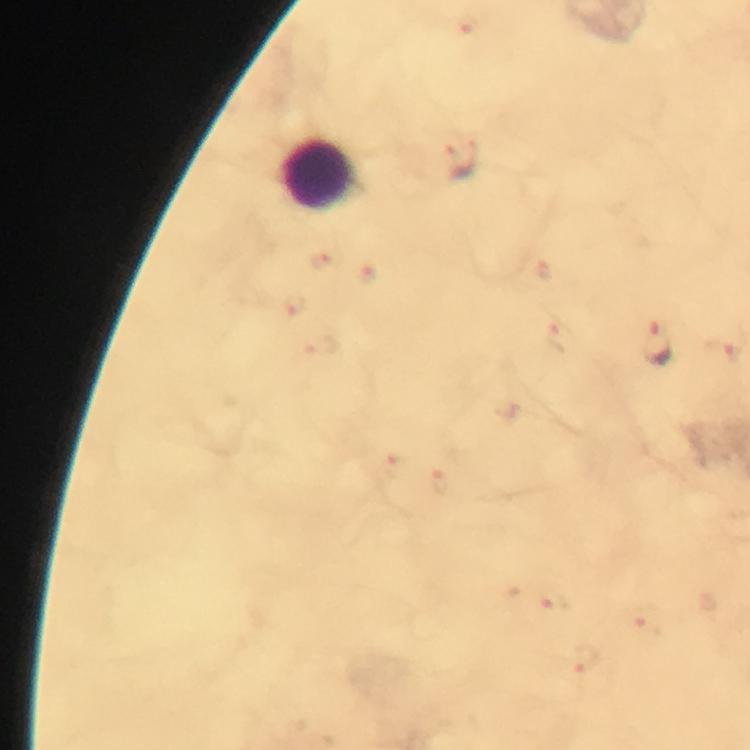

Approximate centers as (x, y) in pixels.
Summary:
  - Leukocyte locations: (321, 179)
  - Malaria parasite locations: (462, 161), (657, 345)
  - Capture: smartphone camera through the microscope
  - Cropped from: one field of view
  - Context: from a diagnostic examination for malaria
  - Stain: Giemsa
  - Preparation: thick smear
  - Image size: 750×750 pixels
  - Magnification: 100x
  - Immersion oil: applied